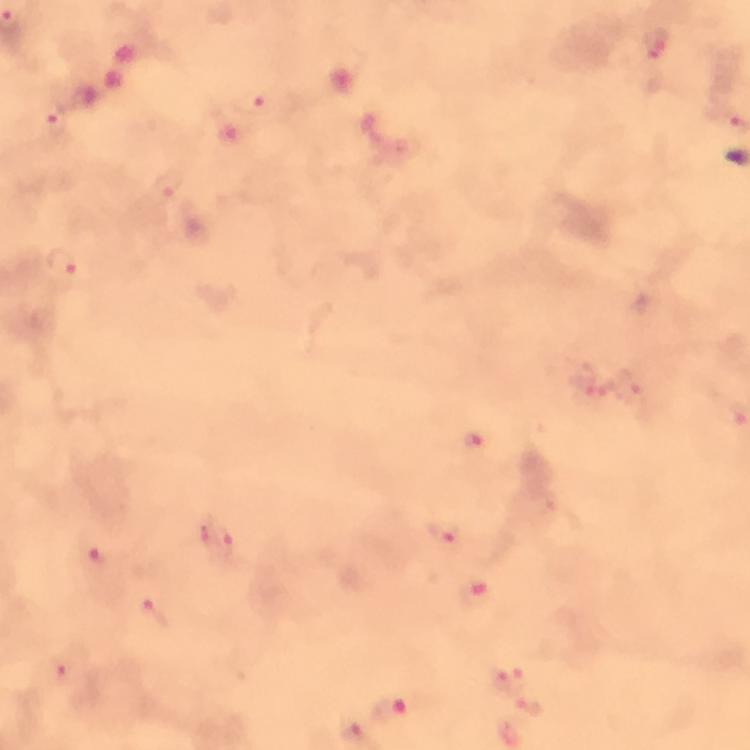
preparation: thick blood film
magnification: 100x
cropped_from: one field of view
immersion_oil: used
capture: smartphone photograph through a microscope
context: from a malaria diagnostic workup
stain: Giemsa
malaria_parasite_locations: 'approximate centers as (x, y) in pixels: (657, 46), (249, 103), (55, 118), (166, 184), (63, 263), (632, 390), (474, 442), (446, 532), (218, 539), (94, 558), (476, 592), (154, 614), (71, 674), (510, 679), (532, 704), (389, 710), (354, 734)'
image_size: 750×750 pixels